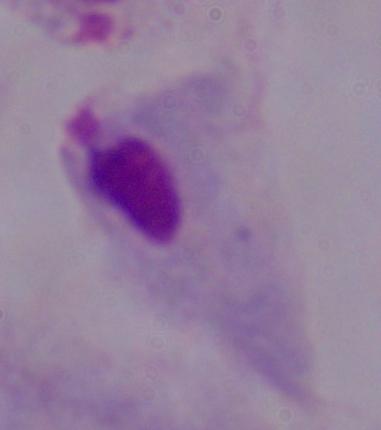

identification = trichomonad
modality = photomicrograph
magnification = 1000x